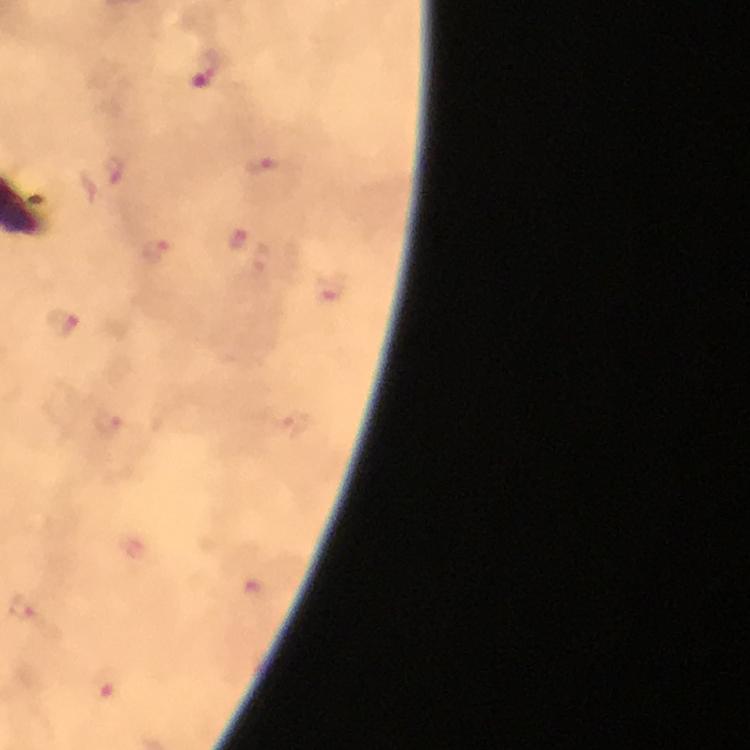
Approximate centers as [x, y] in pixels. Malaria parasite locations: [204, 69], [258, 165], [115, 171], [237, 240], [155, 251], [63, 322], [21, 606], [109, 687]. From a diagnostic examination for malaria. Thick blood smear. Image is 750×750 pixels. Cropped region of a single field of view. Immersion oil was used. Photographed through the microscope with a smartphone camera. At 100x magnification. Giemsa stain.